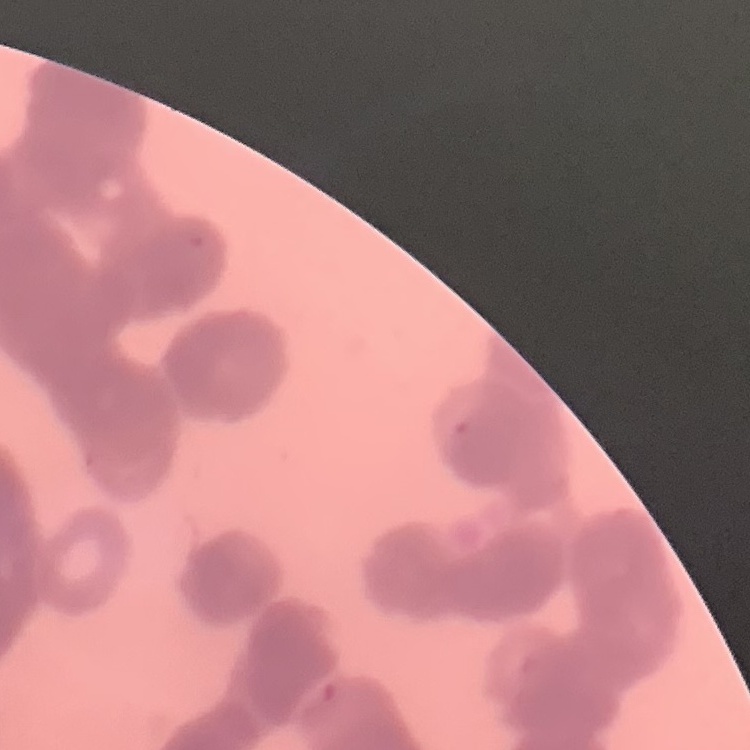
red blood cell morphology = rouleaux formation
stain = Field's or Giemsa
image type = square crop of a larger photomicrograph
preparation = thin blood smear